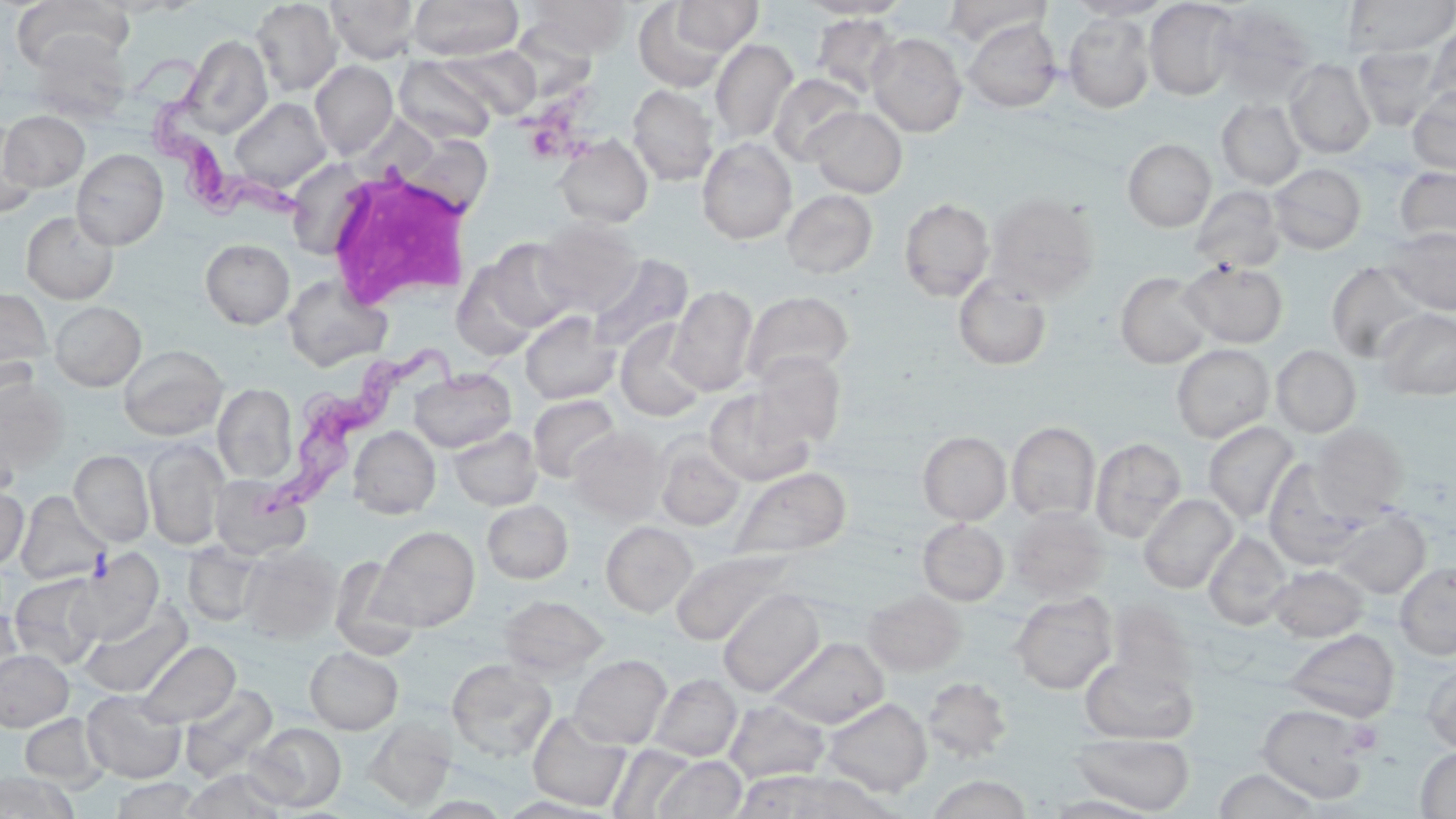
Approximate bounding boxes as [x1, y1, x2, y2] in pixels. Trypanosoma brucei locations: [131, 58, 316, 229], [273, 334, 520, 514]. White blood cell locations: [321, 159, 476, 311]. Uninfected red blood cell locations: [10, 0, 131, 72], [250, 0, 342, 97], [409, 0, 523, 60], [529, 0, 630, 57], [671, 0, 763, 55], [942, 0, 1052, 47], [1065, 0, 1172, 20], [1344, 0, 1456, 56], [325, 1, 420, 63], [799, 1, 910, 19], [1144, 1, 1241, 100], [634, 2, 732, 92], [1209, 4, 1317, 104], [811, 13, 902, 98], [1063, 14, 1156, 113], [963, 19, 1062, 113], [509, 20, 598, 102], [1425, 22, 1456, 110], [28, 31, 131, 122], [867, 32, 967, 137], [182, 35, 273, 138], [710, 38, 799, 145], [1353, 44, 1445, 132], [443, 45, 540, 120], [394, 56, 496, 144], [1284, 59, 1376, 159], [310, 60, 398, 158], [769, 73, 865, 165], [627, 84, 718, 185], [1408, 86, 1456, 175], [230, 97, 331, 192], [1216, 99, 1305, 190], [806, 106, 907, 198], [2, 110, 89, 191], [0, 121, 38, 217], [554, 134, 653, 228], [697, 137, 797, 244], [1123, 139, 1216, 231], [71, 149, 168, 249], [284, 151, 373, 261], [1268, 163, 1367, 254], [1395, 166, 1456, 249], [1190, 185, 1286, 274], [782, 189, 877, 279], [985, 192, 1100, 301], [898, 198, 994, 301], [21, 211, 118, 303], [535, 217, 644, 316], [1385, 226, 1456, 315], [200, 238, 295, 329], [484, 238, 578, 332], [587, 252, 693, 355], [1180, 259, 1289, 348], [451, 260, 542, 361], [1326, 260, 1429, 363], [1116, 271, 1213, 368], [282, 274, 392, 372], [953, 274, 1052, 370], [667, 286, 758, 396], [0, 288, 52, 380], [741, 290, 854, 385], [49, 301, 146, 391], [1374, 308, 1456, 400], [520, 311, 620, 404], [615, 319, 708, 422], [1171, 343, 1274, 443], [118, 344, 227, 440], [1271, 345, 1361, 437], [748, 352, 846, 448], [409, 368, 516, 452], [0, 377, 70, 475], [213, 383, 297, 483], [704, 389, 815, 486], [528, 394, 622, 482], [1007, 421, 1100, 522], [1203, 422, 1300, 525], [1311, 424, 1408, 517], [348, 426, 440, 518], [568, 426, 669, 522], [449, 427, 542, 511], [918, 431, 1011, 525], [1090, 437, 1187, 543], [143, 438, 228, 550], [655, 439, 745, 531], [69, 450, 154, 546], [1262, 459, 1373, 567], [730, 466, 851, 560], [209, 475, 310, 561], [0, 486, 28, 571], [15, 491, 109, 585], [1138, 493, 1238, 594], [482, 499, 573, 583], [1008, 507, 1109, 602], [1331, 507, 1430, 599], [918, 518, 1009, 605], [600, 521, 697, 616], [372, 525, 479, 632], [1204, 531, 1292, 630], [183, 542, 263, 626], [239, 544, 342, 644], [671, 548, 798, 646], [71, 549, 164, 644], [330, 557, 418, 658], [1394, 562, 1456, 660], [1268, 564, 1369, 643], [10, 573, 105, 669], [718, 589, 824, 697], [862, 589, 966, 675], [1010, 592, 1117, 694], [499, 594, 608, 680], [79, 600, 192, 699], [1107, 602, 1199, 690], [0, 606, 23, 693], [1285, 628, 1400, 722], [770, 637, 889, 729], [137, 641, 239, 727], [304, 646, 403, 734], [0, 650, 73, 731], [569, 654, 672, 749], [1080, 657, 1198, 744], [446, 658, 557, 762], [1422, 660, 1456, 754], [649, 673, 741, 761], [922, 677, 1013, 762], [179, 684, 277, 781], [82, 690, 186, 783], [821, 697, 932, 797], [724, 700, 830, 784], [1257, 704, 1372, 803], [528, 712, 630, 811], [20, 713, 109, 790], [363, 715, 456, 811], [248, 722, 346, 811], [1070, 732, 1195, 814], [609, 744, 699, 819], [1415, 747, 1456, 818], [653, 755, 746, 818], [1212, 768, 1325, 818], [182, 769, 288, 819], [732, 770, 847, 818], [0, 772, 77, 818], [774, 772, 894, 818], [927, 775, 1032, 818], [111, 777, 201, 819], [1043, 795, 1160, 818]. Platelet locations: [1347, 720, 1382, 754]. Slide-level diagnosis: Trypanosoma brucei. Captured at 1000x magnification. Image is 1456×819 pixels. Thin blood smear. Light microscopy. May-Grünwald-Giemsa-stained preparation. Single field of view.